Name the parasite shown.
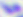
This is Toxoplasma gondii.

Summary:
  - Magnification: 400x
  - Modality: photomicrograph